Locate malaria parasites and leukocytes.
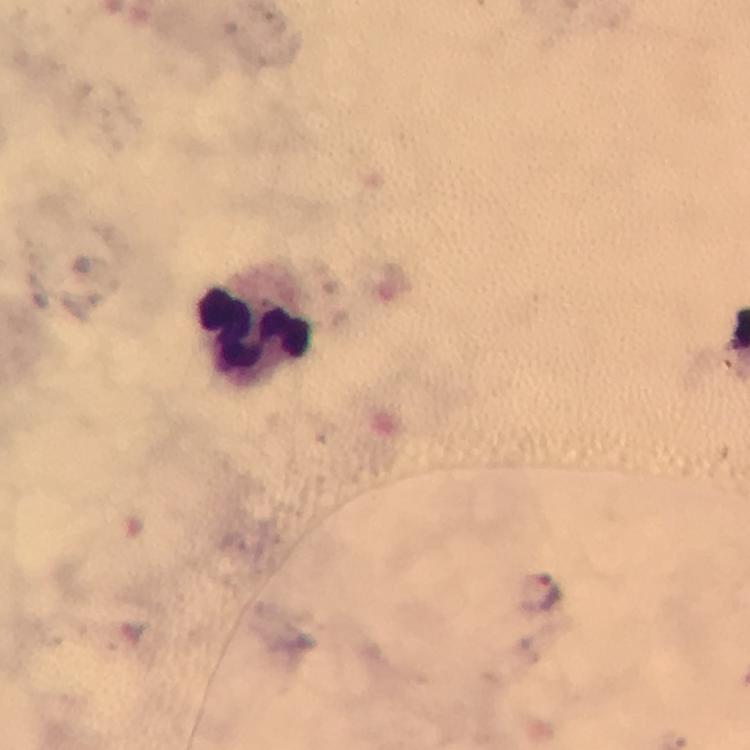

Approximate centers as [x, y] in pixels.
Malaria parasites: [276, 23], [540, 594].
Leukocytes: [254, 329].

Smartphone photograph taken through a microscope. Giemsa-stained preparation. A crop from one field of view. Image is 750×750 pixels. At 100x magnification. From a diagnostic examination for malaria. Thick blood smear. Immersion oil applied.